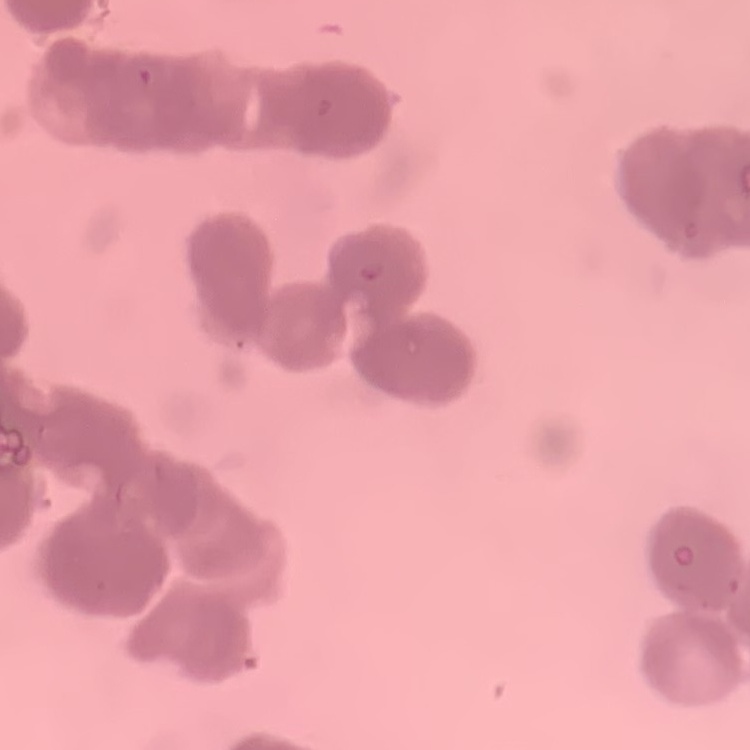
Summary:
  - Erythrocyte morphology: rouleaux formation
  - Image type: one tile cut from a larger photomicrograph
  - Stain: Field's or Giemsa
  - Preparation: thin peripheral smear